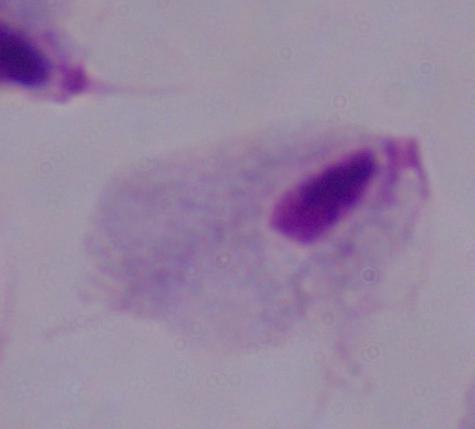
modality = photomicrograph
identification = trichomonad
magnification = 1000x